Describe the morphology of the erythrocytes.
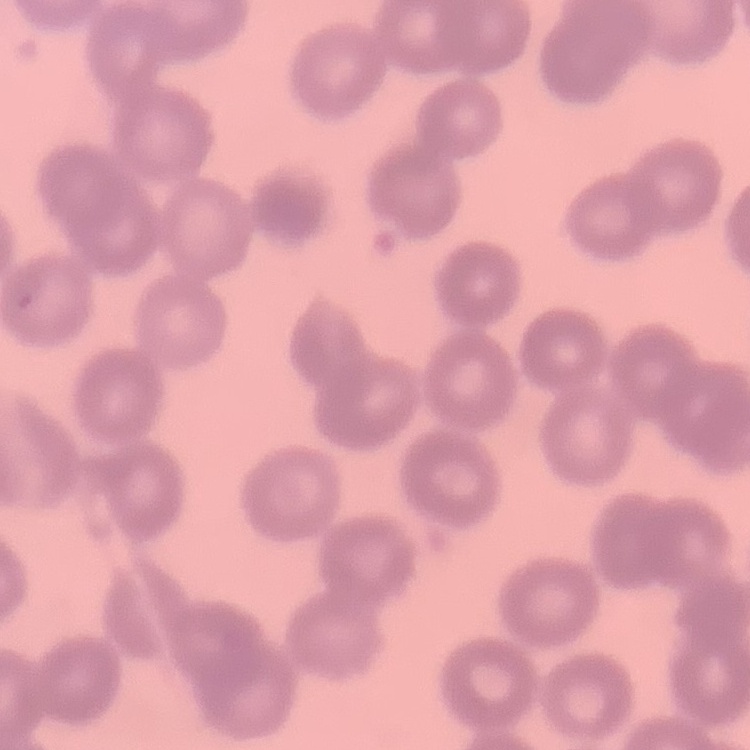

No rouleaux formation.

Summary:
  - Stain: Field's or Giemsa
  - Image type: square crop of a larger photomicrograph
  - Preparation: thin blood smear